Report the malaria status of this cell.
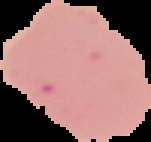

It is uninfected.

image size = 151×142 pixels
image type = segmented cell region on a black background
preparation = thin blood smear